State the blood parasite species.
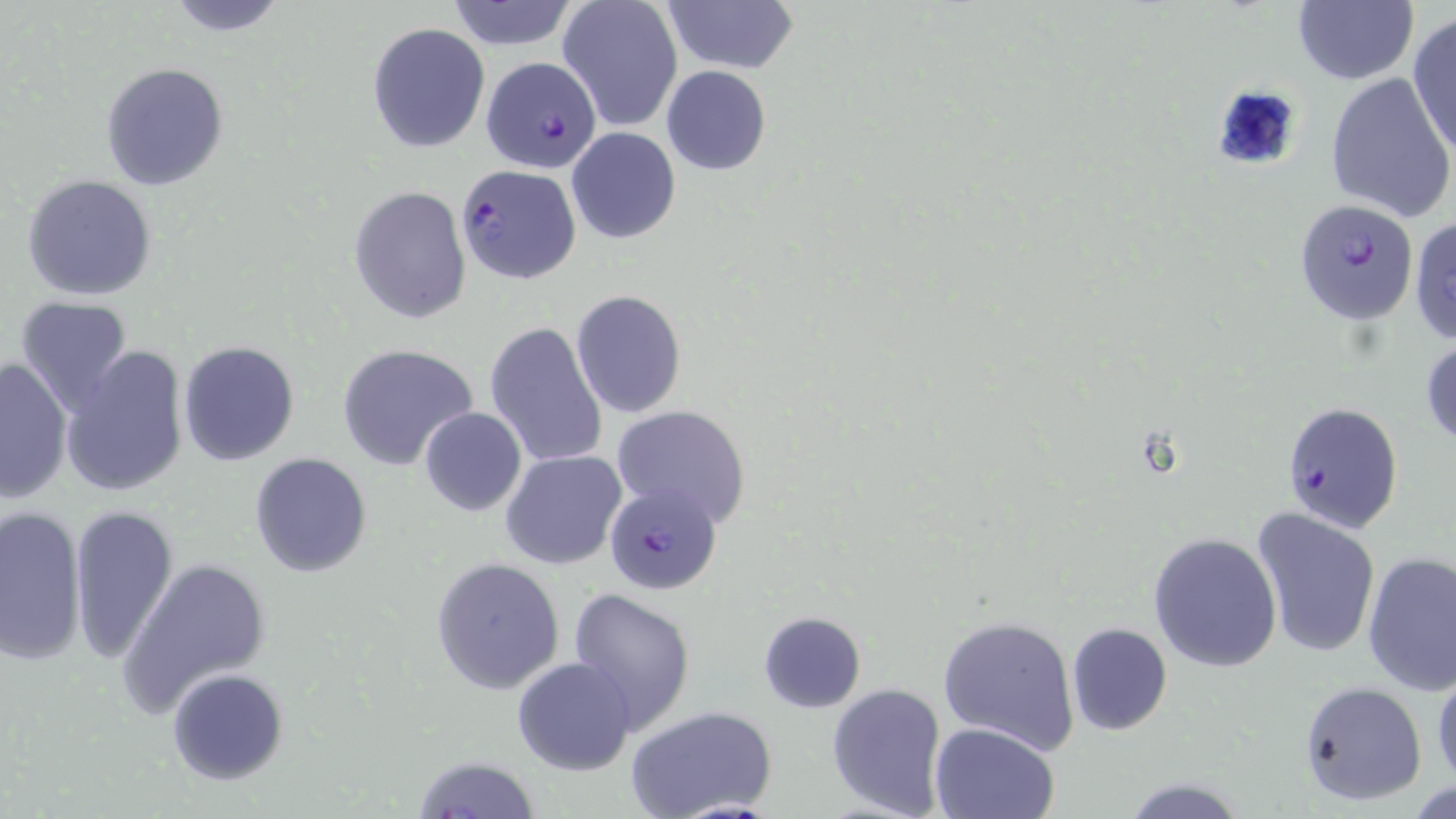
Plasmodium falciparum.

Summary:
  - Coordinate format: approximate bounding boxes as (x1,y1)-(x2,y2) corner pairs in pixels
  - Plasmodium falciparum-infected red blood cell locations: (481,56)-(603,175), (457,165)-(581,282), (1297,203)-(1419,325), (1279,400)-(1404,535), (604,482)-(721,595)
  - Uninfected red blood cell locations: (162,0)-(290,36), (446,0)-(579,51), (660,0)-(799,75), (1293,0)-(1418,85), (559,1)-(683,131), (1408,13)-(1456,160), (367,21)-(490,153), (101,61)-(230,192), (661,66)-(771,175), (1325,71)-(1456,224), (566,126)-(680,244), (22,173)-(157,301), (350,184)-(471,323), (1410,215)-(1456,346), (570,290)-(687,417), (14,297)-(135,415), (485,321)-(609,470), (1420,335)-(1456,451), (178,341)-(301,467), (337,344)-(478,471), (60,345)-(189,498), (1,358)-(72,501), (610,405)-(751,527), (418,407)-(527,516), (501,450)-(627,571), (248,454)-(372,577), (0,504)-(89,669), (67,504)-(177,665), (1251,508)-(1382,660), (1147,531)-(1283,672), (1361,551)-(1456,696), (430,556)-(565,694), (118,558)-(271,715), (567,589)-(695,732), (758,611)-(867,713), (937,615)-(1079,755), (1065,622)-(1173,736), (513,655)-(636,774), (167,667)-(289,785), (1431,667)-(1455,789), (1299,680)-(1428,806), (826,682)-(947,816), (628,707)-(775,819), (930,721)-(1060,818), (411,755)-(541,818), (1121,777)-(1248,817)
  - Field of view: one of a larger specimen
  - Image size: 1456×819 pixels
  - Modality: optical microscopy
  - Magnification: 1000x
  - Stain: May-Grünwald-Giemsa
  - Preparation: thin blood film